Assess this cell for malaria.
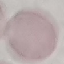
Uninfected.

Automatically extracted cell patch, resized to 64 × 64 pixels. Giemsa-stained preparation. Thin blood film. Photographed with a smartphone camera at the microscope eyepiece.